Outline platelets.
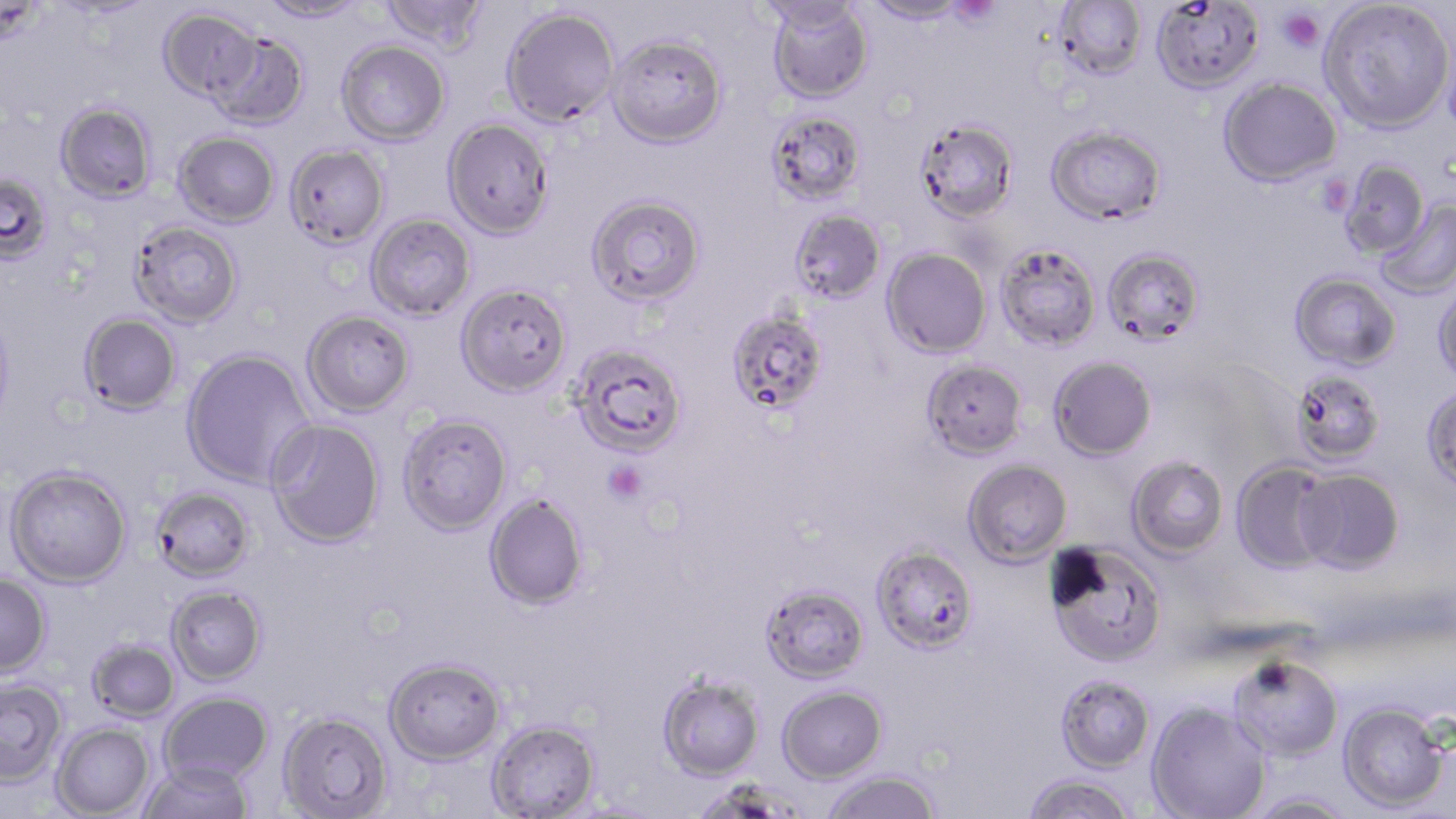

Approximate bounding boxes as named x1/y1/x2/y2 corners in pixels.
Platelets: (x1=947, y1=0, x2=1002, y2=27), (x1=1277, y1=8, x2=1324, y2=53), (x1=602, y1=460, x2=647, y2=504).

Summary:
  - Uninfected red blood cell locations: (x1=257, y1=0, x2=370, y2=24), (x1=380, y1=0, x2=490, y2=53), (x1=862, y1=0, x2=972, y2=26), (x1=1053, y1=0, x2=1148, y2=81), (x1=1319, y1=0, x2=1454, y2=135), (x1=48, y1=1, x2=160, y2=21), (x1=754, y1=1, x2=869, y2=33), (x1=766, y1=1, x2=874, y2=104), (x1=1150, y1=1, x2=1264, y2=95), (x1=158, y1=7, x2=263, y2=104), (x1=501, y1=7, x2=619, y2=127), (x1=206, y1=31, x2=310, y2=130), (x1=607, y1=34, x2=727, y2=148), (x1=337, y1=40, x2=451, y2=146), (x1=1219, y1=77, x2=1342, y2=187), (x1=55, y1=101, x2=157, y2=204), (x1=766, y1=109, x2=867, y2=207), (x1=443, y1=118, x2=554, y2=239), (x1=913, y1=119, x2=1019, y2=223), (x1=1045, y1=125, x2=1167, y2=226), (x1=173, y1=131, x2=280, y2=227), (x1=283, y1=144, x2=389, y2=250), (x1=1339, y1=160, x2=1430, y2=259), (x1=0, y1=170, x2=54, y2=264), (x1=586, y1=194, x2=706, y2=307), (x1=1374, y1=200, x2=1456, y2=299), (x1=789, y1=209, x2=886, y2=305), (x1=365, y1=212, x2=476, y2=321), (x1=129, y1=220, x2=243, y2=328), (x1=994, y1=242, x2=1100, y2=352), (x1=882, y1=248, x2=991, y2=359), (x1=1102, y1=248, x2=1205, y2=346), (x1=1289, y1=271, x2=1402, y2=371), (x1=1432, y1=280, x2=1456, y2=387), (x1=456, y1=282, x2=573, y2=397), (x1=0, y1=307, x2=16, y2=431), (x1=726, y1=308, x2=830, y2=417), (x1=301, y1=310, x2=416, y2=417), (x1=78, y1=312, x2=182, y2=415), (x1=569, y1=343, x2=688, y2=459), (x1=181, y1=348, x2=316, y2=489), (x1=1048, y1=355, x2=1157, y2=461), (x1=921, y1=358, x2=1028, y2=460), (x1=1289, y1=369, x2=1386, y2=466), (x1=1420, y1=385, x2=1456, y2=493), (x1=397, y1=413, x2=512, y2=535), (x1=266, y1=418, x2=385, y2=548), (x1=1127, y1=455, x2=1229, y2=558), (x1=962, y1=459, x2=1073, y2=566), (x1=1231, y1=459, x2=1337, y2=573), (x1=5, y1=464, x2=133, y2=589), (x1=1295, y1=469, x2=1405, y2=574), (x1=151, y1=485, x2=256, y2=582), (x1=484, y1=493, x2=589, y2=611), (x1=1044, y1=541, x2=1168, y2=668), (x1=870, y1=544, x2=978, y2=655), (x1=0, y1=574, x2=52, y2=677), (x1=759, y1=583, x2=870, y2=684), (x1=165, y1=585, x2=267, y2=686), (x1=86, y1=638, x2=180, y2=723), (x1=384, y1=656, x2=506, y2=764), (x1=1228, y1=656, x2=1343, y2=761), (x1=1055, y1=673, x2=1155, y2=773), (x1=657, y1=674, x2=764, y2=780), (x1=0, y1=677, x2=68, y2=785), (x1=777, y1=685, x2=887, y2=783), (x1=159, y1=692, x2=273, y2=785), (x1=1338, y1=701, x2=1450, y2=813), (x1=1146, y1=702, x2=1270, y2=819), (x1=277, y1=709, x2=392, y2=818), (x1=486, y1=718, x2=601, y2=818), (x1=52, y1=722, x2=155, y2=818), (x1=138, y1=759, x2=254, y2=819), (x1=821, y1=769, x2=941, y2=819), (x1=1023, y1=774, x2=1138, y2=819), (x1=1247, y1=792, x2=1357, y2=819)
  - Slide-level diagnosis: Plasmodium falciparum
  - Modality: light microscopy
  - Preparation: thin blood smear
  - Field of view: one of a larger specimen
  - Magnification: 1000x
  - Stain: May-Grünwald-Giemsa
  - Image size: 1456×819 pixels